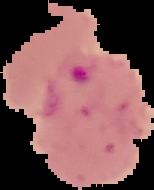

Summary:
  - Preparation: thin blood smear
  - Image size: 154×190 pixels
  - Result: malaria parasites detected
  - Image type: cell region segmented out of the field of view; surrounding area masked to black